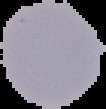
Summary:
  - Image type: cell region segmented out of the field of view; surrounding area masked to black
  - Image size: 106×109 pixels
  - Result: no malaria parasites seen
  - Preparation: thin blood film